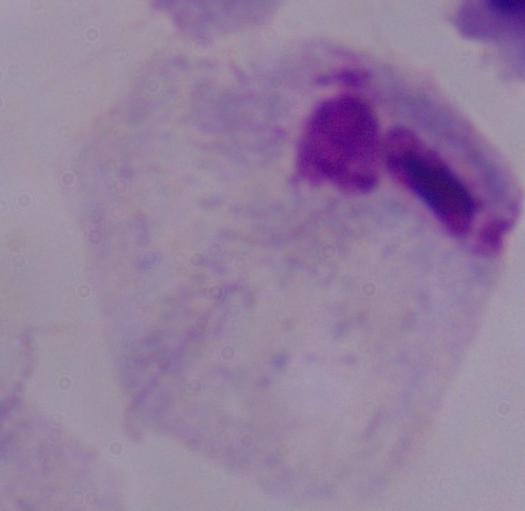 A trichomonad is seen. Captured at 1000x magnification. Micrograph.